Outline every malaria parasite.
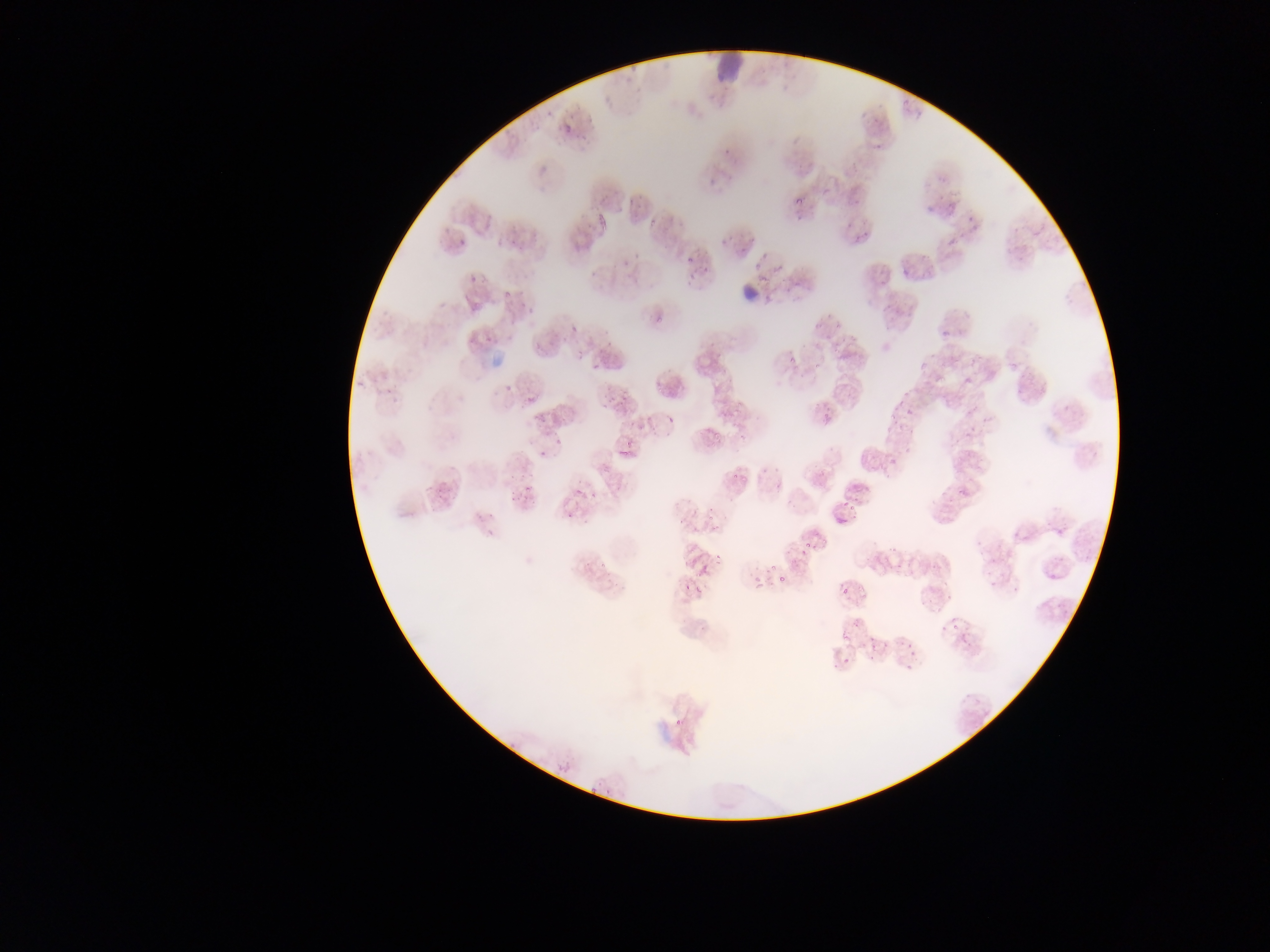

No malaria parasites observed.

{
  "leukocyte_locations": "approximate bounding boxes as (left, top, right, bottom) in pixels: (702, 50, 761, 78)",
  "field_of_view": "single",
  "image_size": "1270×952 pixels",
  "capture": "mobile-phone photograph through a microscope",
  "preparation": "thin blood smear",
  "country": "Ghana"
}